Report the malaria status of this cell.
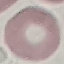

Uninfected.

preparation = thin blood smear
capture = smartphone camera at the microscope eyepiece
stain = Giemsa
image type = automatically extracted cell patch, resized to 64 × 64 pixels